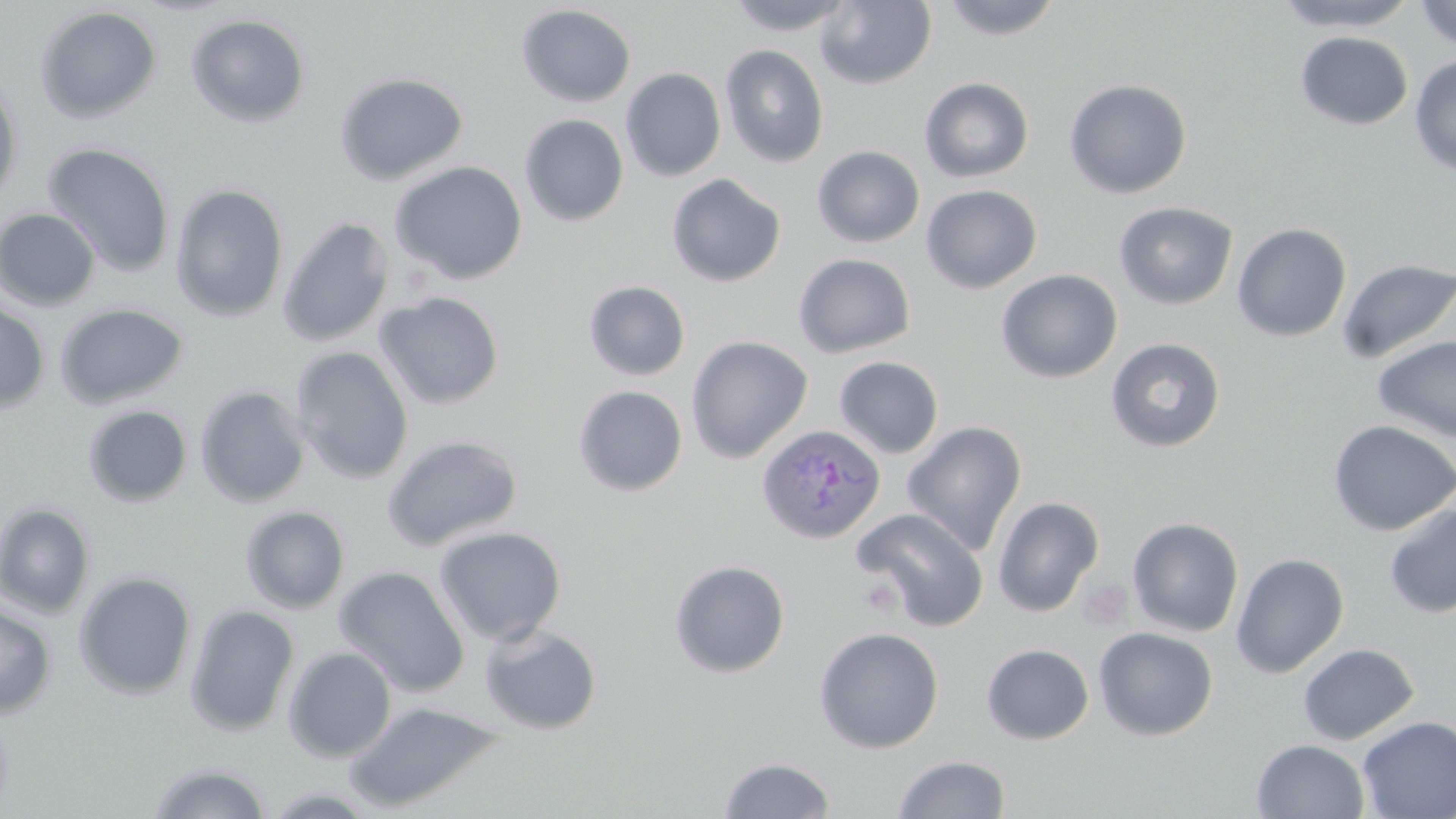

Approximate bounding boxes as (x1, y1, x2, y2) in pixels. Platelet locations: (1079, 578, 1132, 629). Uninfected red blood cell locations: (724, 0, 855, 35), (815, 0, 936, 89), (938, 0, 1064, 40), (1272, 0, 1421, 33), (1413, 0, 1456, 51), (516, 4, 636, 108), (34, 5, 162, 123), (185, 13, 311, 128), (1295, 31, 1413, 131), (719, 44, 829, 168), (1409, 54, 1456, 176), (620, 68, 726, 182), (334, 72, 468, 185), (0, 76, 24, 208), (919, 77, 1034, 182), (1064, 78, 1192, 198), (519, 114, 629, 226), (41, 142, 176, 278), (812, 145, 925, 248), (390, 161, 528, 285), (666, 173, 786, 287), (170, 183, 289, 322), (920, 185, 1042, 294), (1114, 201, 1238, 310), (0, 208, 101, 311), (277, 216, 394, 347), (1232, 223, 1351, 342), (793, 253, 915, 358), (1335, 257, 1455, 365), (995, 269, 1122, 384), (583, 281, 690, 381), (374, 291, 504, 410), (0, 299, 51, 414), (54, 302, 189, 409), (685, 335, 813, 464), (1371, 335, 1456, 445), (1105, 337, 1226, 453), (290, 346, 413, 484), (834, 356, 944, 458), (194, 386, 310, 508), (573, 386, 688, 496), (82, 405, 193, 508), (1327, 419, 1455, 536), (902, 421, 1027, 556), (381, 435, 523, 551), (992, 496, 1103, 617), (0, 502, 96, 619), (1383, 502, 1456, 619), (240, 505, 350, 614), (852, 508, 989, 631), (1127, 517, 1244, 637), (434, 526, 567, 647), (1231, 552, 1349, 678), (669, 560, 790, 678), (333, 566, 470, 697), (73, 570, 196, 701), (0, 600, 57, 718), (184, 603, 300, 737), (478, 623, 603, 734), (813, 627, 944, 754), (1093, 627, 1218, 740), (981, 643, 1094, 745), (1297, 643, 1420, 745), (283, 647, 397, 762), (342, 700, 506, 813), (1357, 716, 1456, 818), (1252, 739, 1370, 819), (892, 755, 1011, 818), (718, 757, 836, 818), (147, 761, 272, 819), (260, 787, 385, 818). Plasmodium ovale-infected red blood cell locations: (757, 424, 885, 545). Slide-level diagnosis: Plasmodium ovale. Single field of view. Image is 1456×819 pixels. May-Grünwald-Giemsa stain. Optical microscopy. Thin blood film. Captured at 1000x magnification.